Locate every malaria parasite.
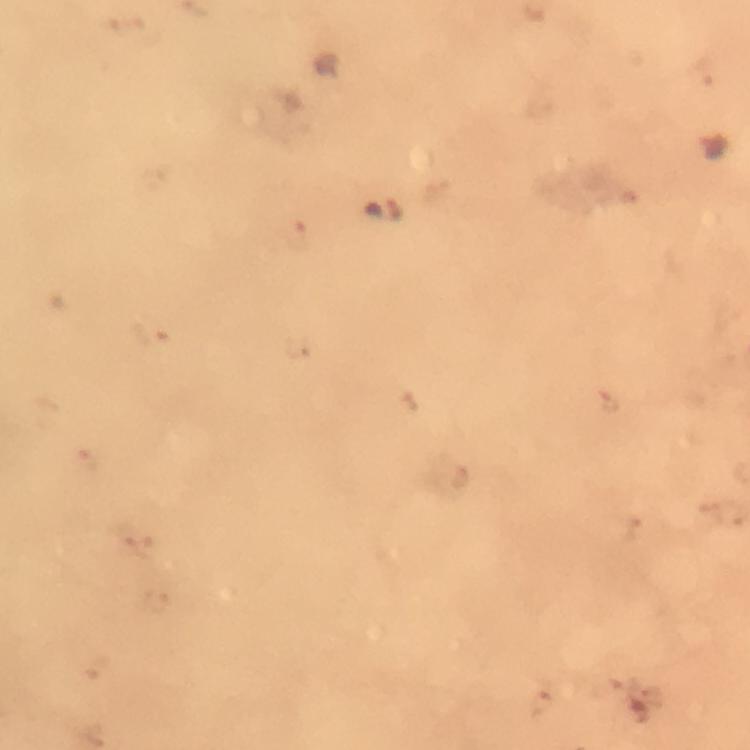

Approximate centers as [x, y] in pixels.
Malaria parasites: [713, 145].

capture = smartphone camera through the microscope
preparation = thick blood film
image size = 750×750 pixels
cropped from = one field of view
context = from a malaria diagnostic workup
immersion oil = used
magnification = 100x
stain = Giemsa